Report the malaria status of this cell.
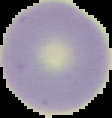
Uninfected.

Image is 112×118 pixels. From a thin blood film. Cell region segmented out of the field of view; the surrounding area is masked to black.